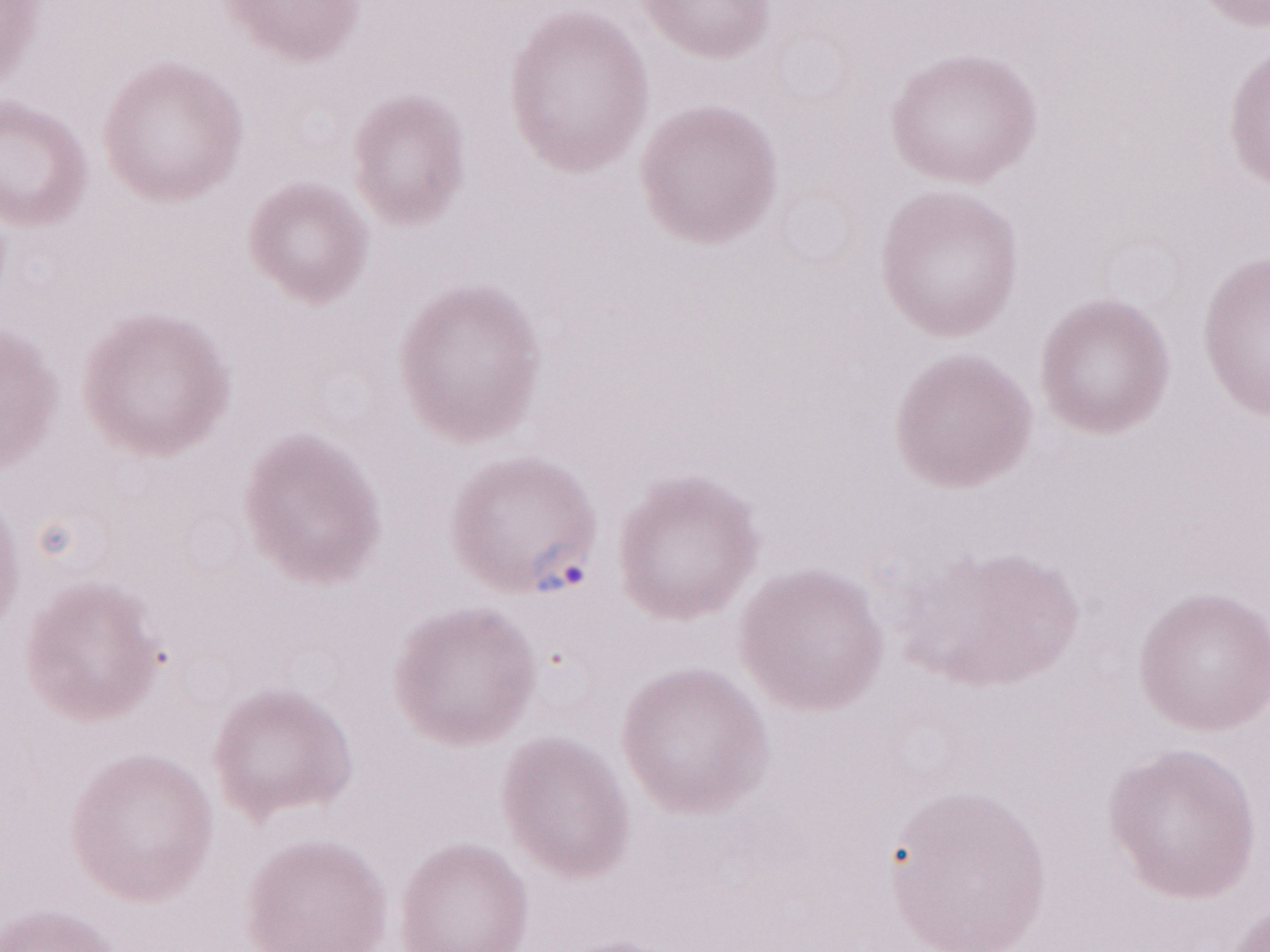
Magnification: 1,000x. Image is 1270×952 pixels. Thin blood film. May-Grünwald-Giemsa (MGG) stain. Olympus BX43 microscope, Olympus DP73 camera. Single field of view. Patient-level malaria diagnosis: positive.